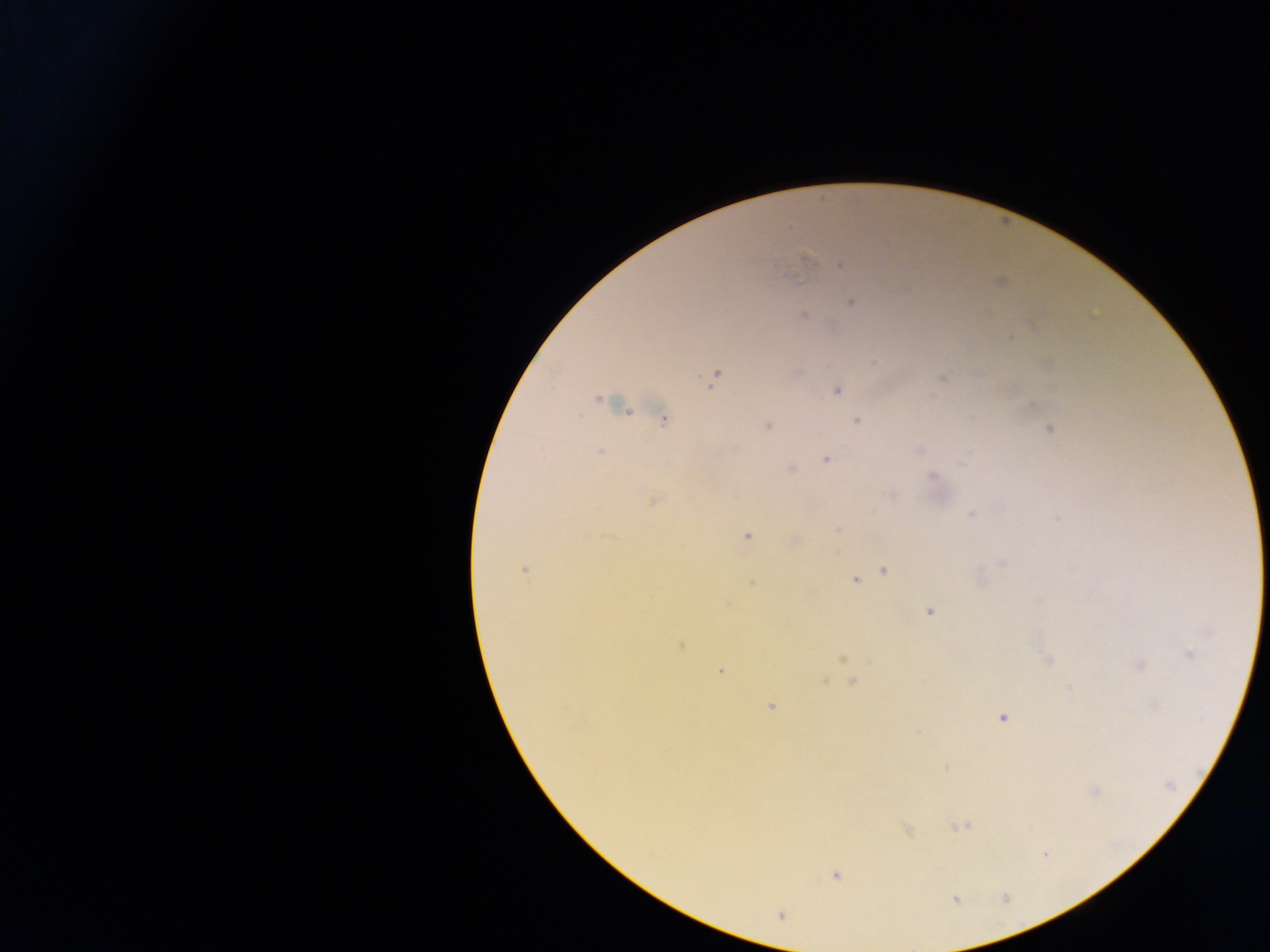

Plasmodium parasite locations = approximate centers as [x, y] in pixels: [806, 258], [840, 265], [789, 277], [852, 302], [804, 317], [873, 363], [714, 376], [837, 390], [598, 399], [663, 419], [856, 421], [766, 426], [1049, 430], [919, 450], [600, 451], [968, 455], [826, 459], [790, 469], [933, 476], [891, 495], [653, 500], [971, 515], [747, 537], [1002, 564], [524, 570], [884, 570], [855, 580], [752, 583], [930, 611], [680, 646], [1190, 654], [842, 658], [1048, 660], [1139, 664], [720, 671], [852, 682], [771, 707], [1003, 717], [918, 732], [1095, 791], [961, 826], [907, 830], [1045, 853], [836, 875], [779, 914]
capture = mobile-phone photograph through a microscope
preparation = thick blood film
field of view = single
image size = 1270×952 pixels
country = Ghana